Give a bounding box for every parasitised red blood cell.
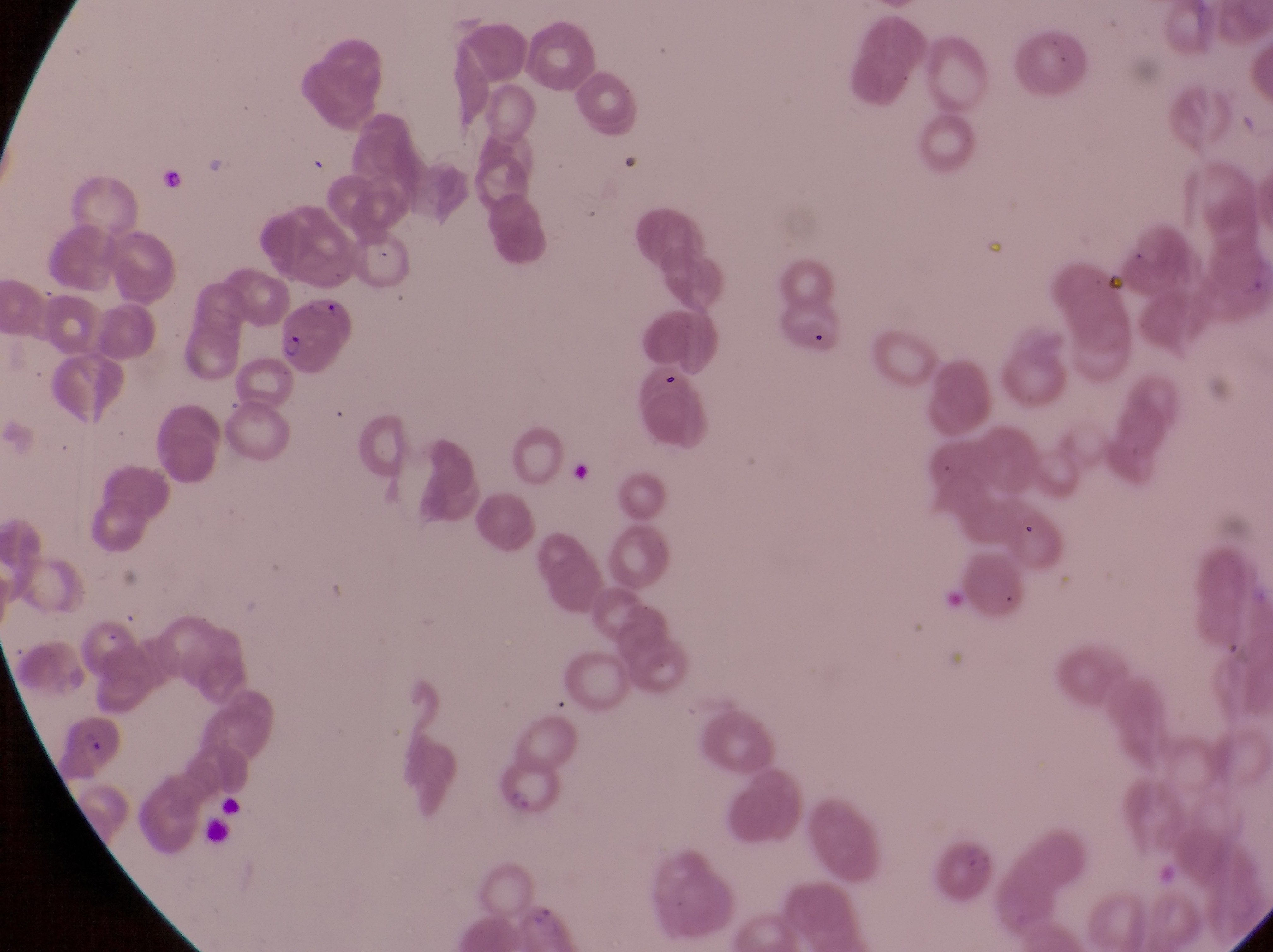
Approximate bounding boxes as left top right bottom in pixels.
Parasitised red blood cells: 277 290 354 370; 58 714 125 782.

capture = smartphone photograph through the eyepiece of an Olympus CX-23 microscope
preparation = thin blood film
field of view = single
country = Uganda
image size = 1273×952 pixels
artifact (platelet-like body, stain precipitate, or debris) locations = approximate bounding boxes as left top right bottom in pixels: 652 367 682 397
magnification = 1000x